Name the cell type shown.
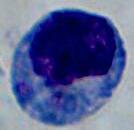
This is a leukocyte.

modality = photomicrograph
magnification = 1000x